Describe the morphology of the erythrocytes.
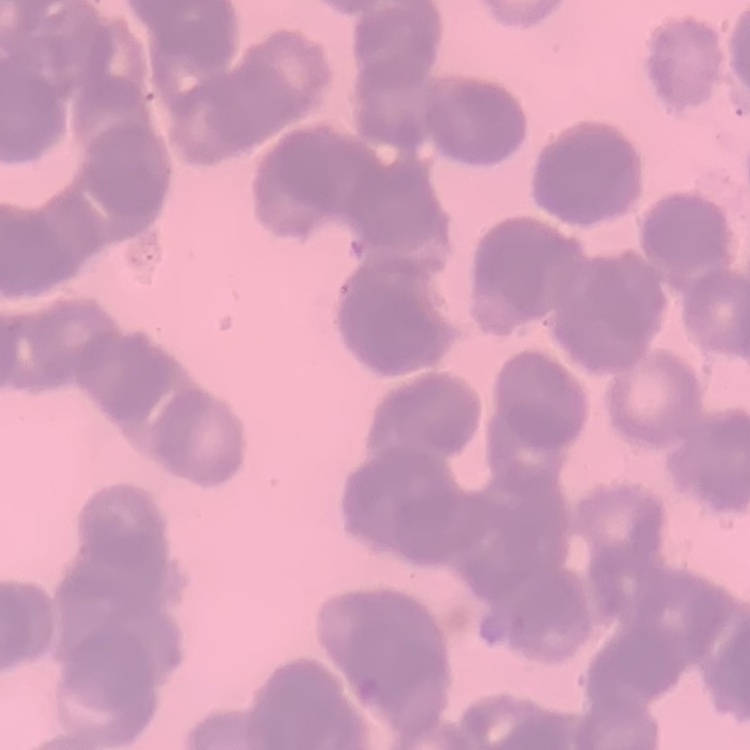
Rouleaux formation.

stain = Field's or Giemsa
image type = square crop of a larger photomicrograph
preparation = thin blood film